Name the parasite shown.
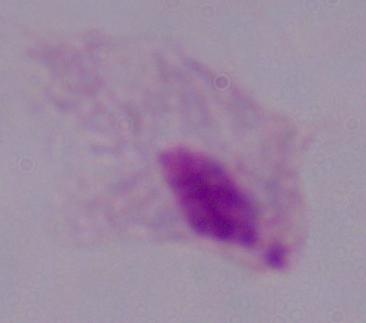

This is a trichomonad.

modality = micrograph
magnification = 1000x